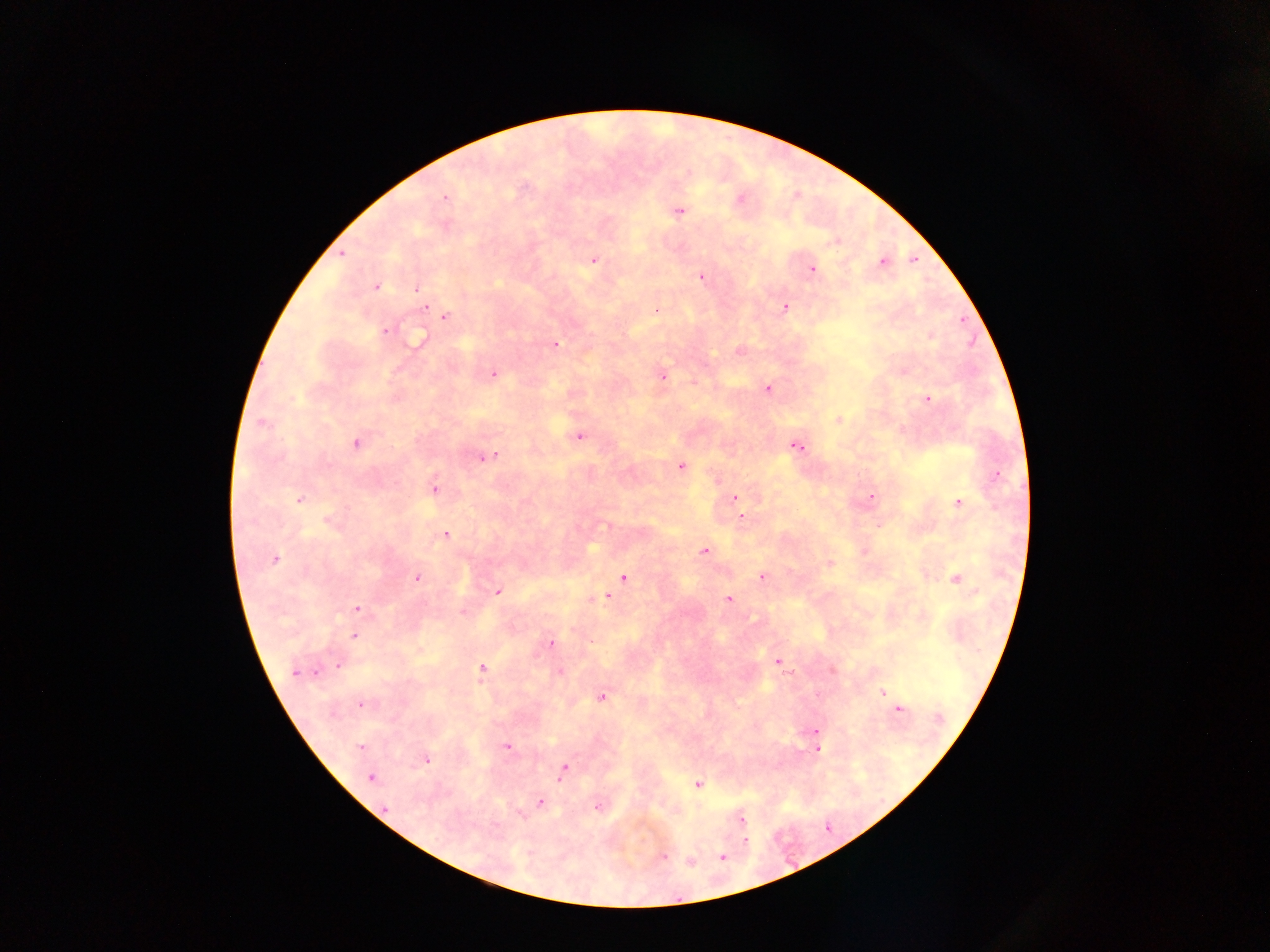
preparation: thick blood smear
capture: mobile-phone photograph through a microscope
image_size: 1270×952 pixels
field_of_view: single
malaria_parasite_locations: 'approximate centers as (x, y) in pixels: (686, 171), (525, 187), (445, 197), (678, 210), (836, 242), (342, 254), (913, 259), (592, 260), (882, 261), (812, 269), (701, 276), (376, 286), (416, 288), (426, 305), (784, 307), (656, 310), (445, 316), (385, 330), (930, 336), (419, 339), (555, 344), (739, 350), (493, 374), (661, 375), (767, 388), (927, 399), (838, 420), (262, 422), (579, 435), (356, 443), (795, 446), (486, 455), (681, 465), (996, 474), (434, 488), (870, 497), (734, 498), (299, 499), (957, 502), (740, 517), (329, 522), (877, 525), (445, 534), (704, 551), (274, 560), (828, 563), (762, 576), (417, 577), (623, 577), (956, 578), (497, 590), (607, 597), (728, 598), (356, 609), (462, 611), (922, 616), (354, 635), (550, 643), (777, 661), (339, 663), (482, 668), (831, 669), (297, 671), (558, 672), (882, 692), (602, 697), (360, 703), (897, 709), (814, 731), (816, 740), (506, 746), (361, 747), (817, 749), (425, 759), (563, 771), (370, 778), (698, 784), (539, 803), (596, 807), (741, 820), (744, 841), (662, 856), (721, 857), (690, 861)'
country: Ghana